Assess this cell for malaria.
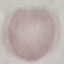
Uninfected.

preparation: thin blood film
capture: smartphone through the microscope eyepiece
stain: Giemsa
image_type: cell patch, automatically extracted from a larger field of view and resized to 64 × 64 pixels